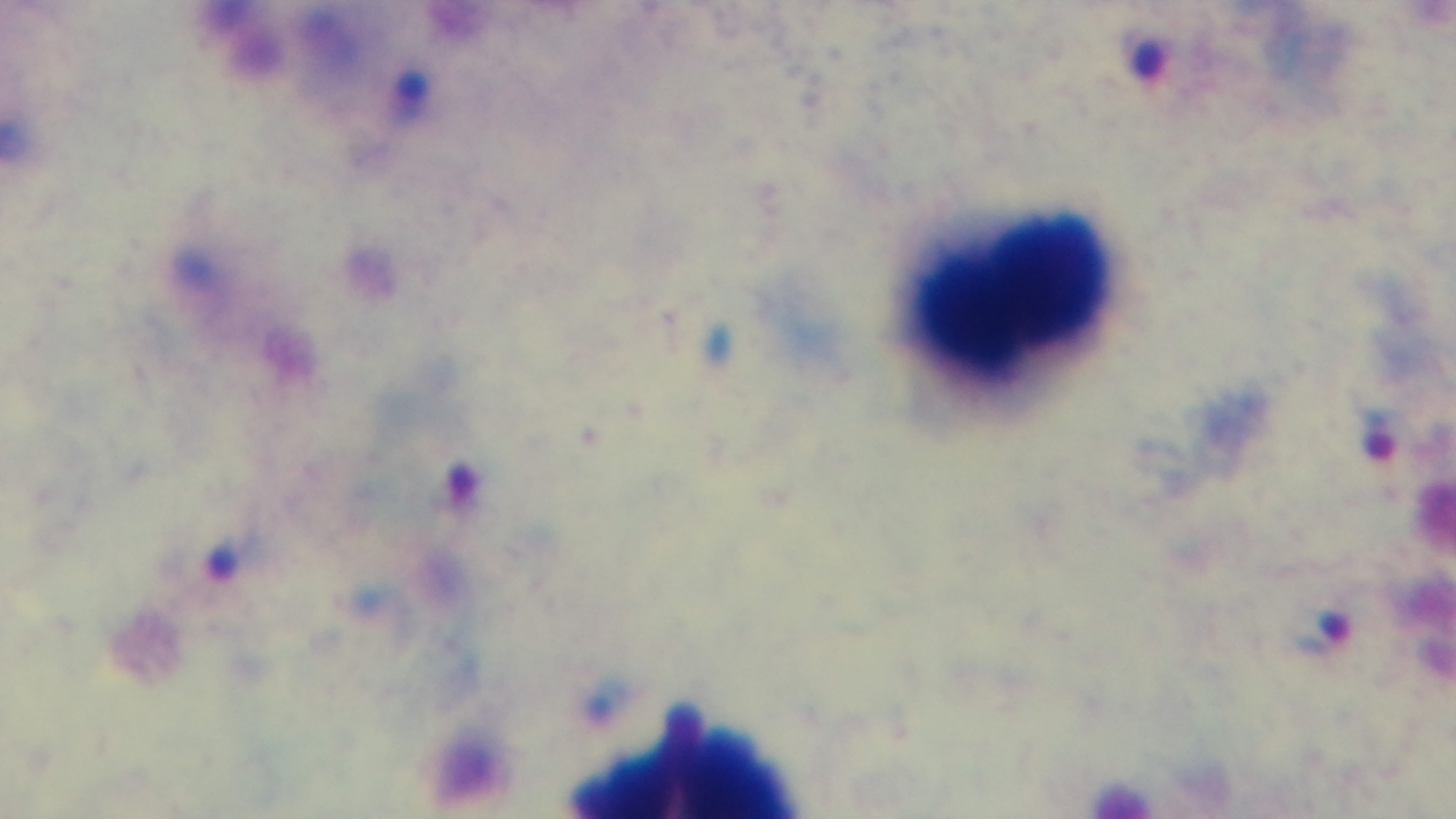
Summary:
  - Stain: Giemsa
  - Capture: mounted 4K digital camera
  - Objective: 100x oil immersion
  - Modality: light microscopy
  - Preparation: thick
  - Field of view: one from the slide
  - Malaria status: positive